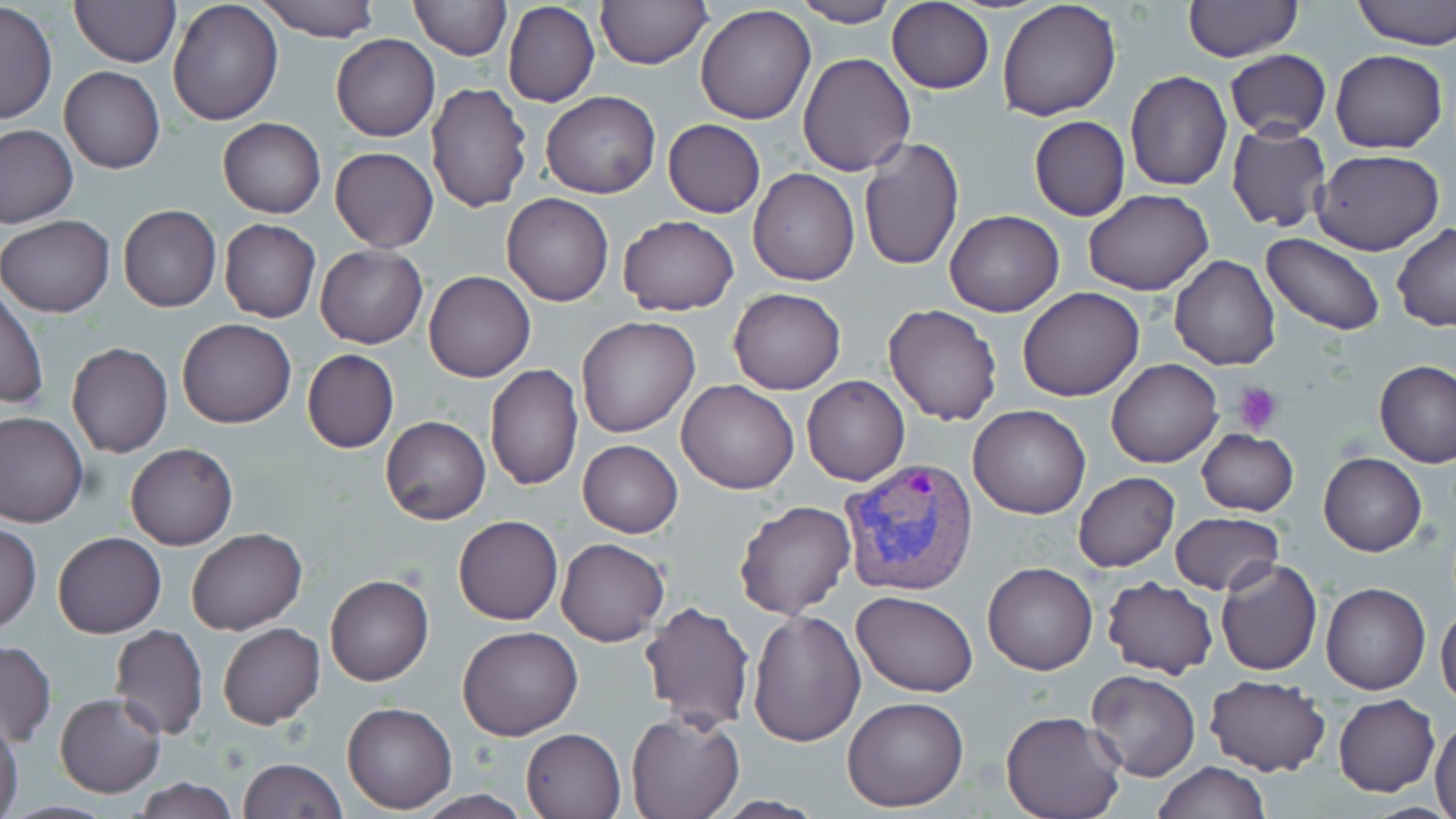

Summary:
  - Coordinate format: approximate bounding boxes as named x1/y1/x2/y2 corners in pixels
  - Platelet locations: (x1=1235, y1=382, x2=1282, y2=434)
  - Plasmodium vivax-infected red blood cell locations: (x1=838, y1=457, x2=980, y2=597)
  - Uninfected red blood cell locations: (x1=257, y1=0, x2=380, y2=41), (x1=408, y1=0, x2=510, y2=60), (x1=595, y1=0, x2=711, y2=68), (x1=997, y1=0, x2=1122, y2=121), (x1=1351, y1=0, x2=1456, y2=48), (x1=69, y1=1, x2=179, y2=67), (x1=167, y1=1, x2=283, y2=124), (x1=502, y1=1, x2=599, y2=107), (x1=792, y1=1, x2=897, y2=27), (x1=887, y1=1, x2=994, y2=94), (x1=1182, y1=1, x2=1302, y2=63), (x1=0, y1=3, x2=57, y2=123), (x1=696, y1=5, x2=817, y2=125), (x1=331, y1=34, x2=439, y2=141), (x1=1331, y1=48, x2=1447, y2=153), (x1=1225, y1=50, x2=1330, y2=140), (x1=796, y1=53, x2=915, y2=176), (x1=59, y1=66, x2=164, y2=175), (x1=1125, y1=71, x2=1233, y2=191), (x1=426, y1=81, x2=533, y2=214), (x1=540, y1=92, x2=660, y2=199), (x1=1028, y1=116, x2=1130, y2=221), (x1=218, y1=117, x2=326, y2=219), (x1=662, y1=119, x2=765, y2=219), (x1=1226, y1=122, x2=1332, y2=233), (x1=1, y1=125, x2=76, y2=228), (x1=857, y1=137, x2=964, y2=271), (x1=330, y1=147, x2=438, y2=252), (x1=1311, y1=149, x2=1445, y2=256), (x1=748, y1=168, x2=859, y2=287), (x1=1083, y1=188, x2=1214, y2=294), (x1=501, y1=194, x2=614, y2=305), (x1=118, y1=205, x2=221, y2=312), (x1=943, y1=210, x2=1065, y2=317), (x1=1, y1=215, x2=114, y2=316), (x1=617, y1=215, x2=739, y2=315), (x1=219, y1=219, x2=321, y2=323), (x1=1392, y1=222, x2=1456, y2=332), (x1=220, y1=231, x2=427, y2=330), (x1=1261, y1=233, x2=1384, y2=336), (x1=314, y1=246, x2=427, y2=348), (x1=1169, y1=254, x2=1281, y2=370), (x1=423, y1=271, x2=535, y2=382), (x1=1017, y1=286, x2=1146, y2=401), (x1=1, y1=288, x2=48, y2=411), (x1=728, y1=288, x2=845, y2=395), (x1=882, y1=303, x2=1003, y2=426), (x1=576, y1=317, x2=700, y2=438), (x1=178, y1=318, x2=296, y2=427), (x1=68, y1=341, x2=172, y2=458), (x1=302, y1=349, x2=399, y2=453), (x1=1105, y1=358, x2=1223, y2=468), (x1=1375, y1=359, x2=1456, y2=468), (x1=484, y1=363, x2=583, y2=490), (x1=803, y1=375, x2=909, y2=486), (x1=676, y1=379, x2=799, y2=494), (x1=967, y1=404, x2=1091, y2=518), (x1=0, y1=412, x2=89, y2=528), (x1=380, y1=415, x2=490, y2=524), (x1=1198, y1=429, x2=1299, y2=516), (x1=578, y1=439, x2=683, y2=537), (x1=126, y1=443, x2=237, y2=550), (x1=1319, y1=452, x2=1427, y2=556), (x1=1074, y1=472, x2=1180, y2=573), (x1=733, y1=500, x2=857, y2=619), (x1=1171, y1=512, x2=1282, y2=595), (x1=454, y1=514, x2=563, y2=625), (x1=0, y1=522, x2=41, y2=632), (x1=186, y1=527, x2=307, y2=634), (x1=53, y1=532, x2=166, y2=638), (x1=555, y1=537, x2=669, y2=648), (x1=1216, y1=558, x2=1322, y2=676), (x1=983, y1=563, x2=1098, y2=675), (x1=325, y1=574, x2=433, y2=686), (x1=1101, y1=577, x2=1218, y2=678), (x1=1321, y1=582, x2=1431, y2=695), (x1=852, y1=590, x2=978, y2=696), (x1=639, y1=601, x2=756, y2=732), (x1=1436, y1=602, x2=1456, y2=705), (x1=747, y1=609, x2=865, y2=745), (x1=217, y1=623, x2=325, y2=729), (x1=108, y1=624, x2=209, y2=740), (x1=457, y1=626, x2=583, y2=740), (x1=1, y1=640, x2=56, y2=745), (x1=1086, y1=670, x2=1199, y2=782), (x1=1203, y1=675, x2=1330, y2=776), (x1=55, y1=692, x2=165, y2=797), (x1=842, y1=695, x2=970, y2=811), (x1=1333, y1=695, x2=1439, y2=796), (x1=342, y1=701, x2=457, y2=814), (x1=1001, y1=708, x2=1126, y2=819), (x1=625, y1=711, x2=744, y2=819), (x1=1431, y1=715, x2=1456, y2=819), (x1=0, y1=716, x2=24, y2=819), (x1=520, y1=727, x2=626, y2=819), (x1=238, y1=758, x2=346, y2=818), (x1=1151, y1=760, x2=1272, y2=818), (x1=134, y1=778, x2=240, y2=818), (x1=709, y1=796, x2=830, y2=817)
  - Slide-level diagnosis: Plasmodium vivax
  - Field of view: one of a larger specimen
  - Magnification: 1000x
  - Stain: May-Grünwald-Giemsa
  - Preparation: thin blood smear
  - Image size: 1456×819 pixels
  - Modality: light microscopy